Describe the morphology of the erythrocytes.
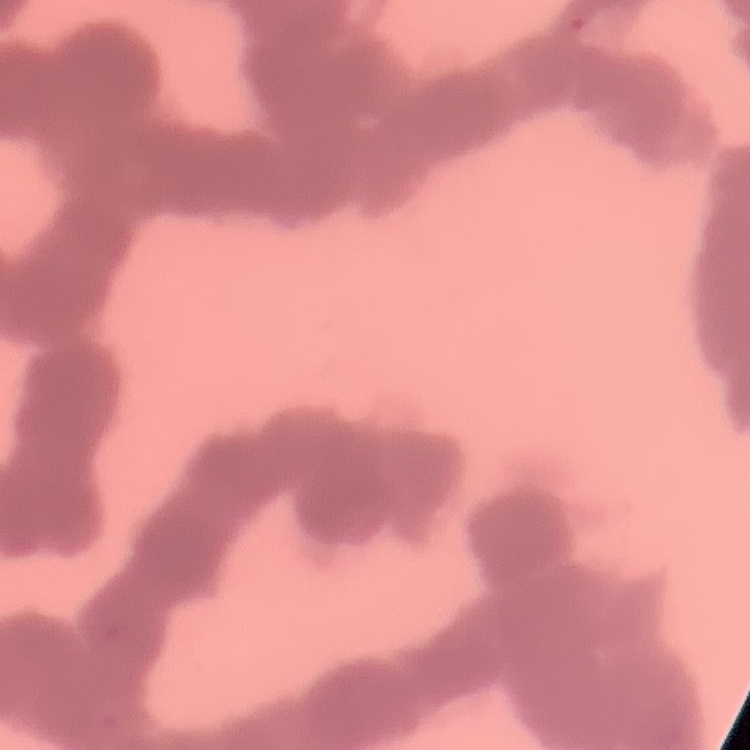
They show rouleaux formation.

Summary:
  - Stain: Field's or Giemsa
  - Preparation: thin peripheral smear
  - Image type: one tile cut from a larger photomicrograph